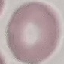
Result: no malaria parasites detected. Photographed with a smartphone camera at the microscope eyepiece. Thin blood smear. Giemsa stain. Automatically extracted cell patch, resized to 64 × 64 pixels.